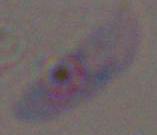
Toxoplasma gondii is seen. Micrograph. Captured at 1000x magnification.